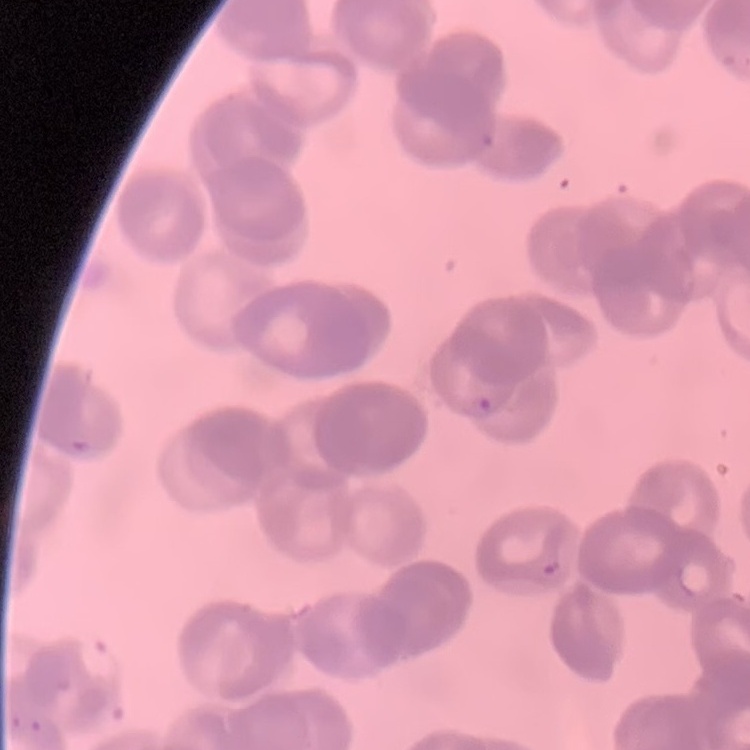

Summary:
  - Erythrocyte morphology: rouleaux formation
  - Stain: Field's or Giemsa
  - Preparation: thin blood film
  - Image type: one tile cut from a larger photomicrograph